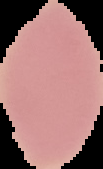

Summary:
  - Image type: cell region segmented out of the field of view; surrounding area masked to black
  - Preparation: thin blood film
  - Image size: 103×169 pixels
  - Result: no malaria parasites seen